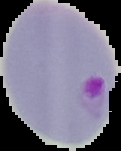

From a thin blood smear. Result: malaria parasites detected. Image is 121×151 pixels. Segmented cell region on a black background.